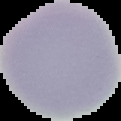
Summary:
  - Image type: cell region segmented out of the field of view; surrounding area masked to black
  - Image size: 121×121 pixels
  - Malaria status: uninfected
  - Preparation: thin blood film